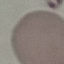

Result: no malaria parasites seen. Thin blood film. Cell patch, automatically extracted from a larger field of view and resized to 64 × 64 pixels. Acquired by smartphone through the microscope eyepiece. Giemsa stain.